Locate every blood parasite and identify its species.
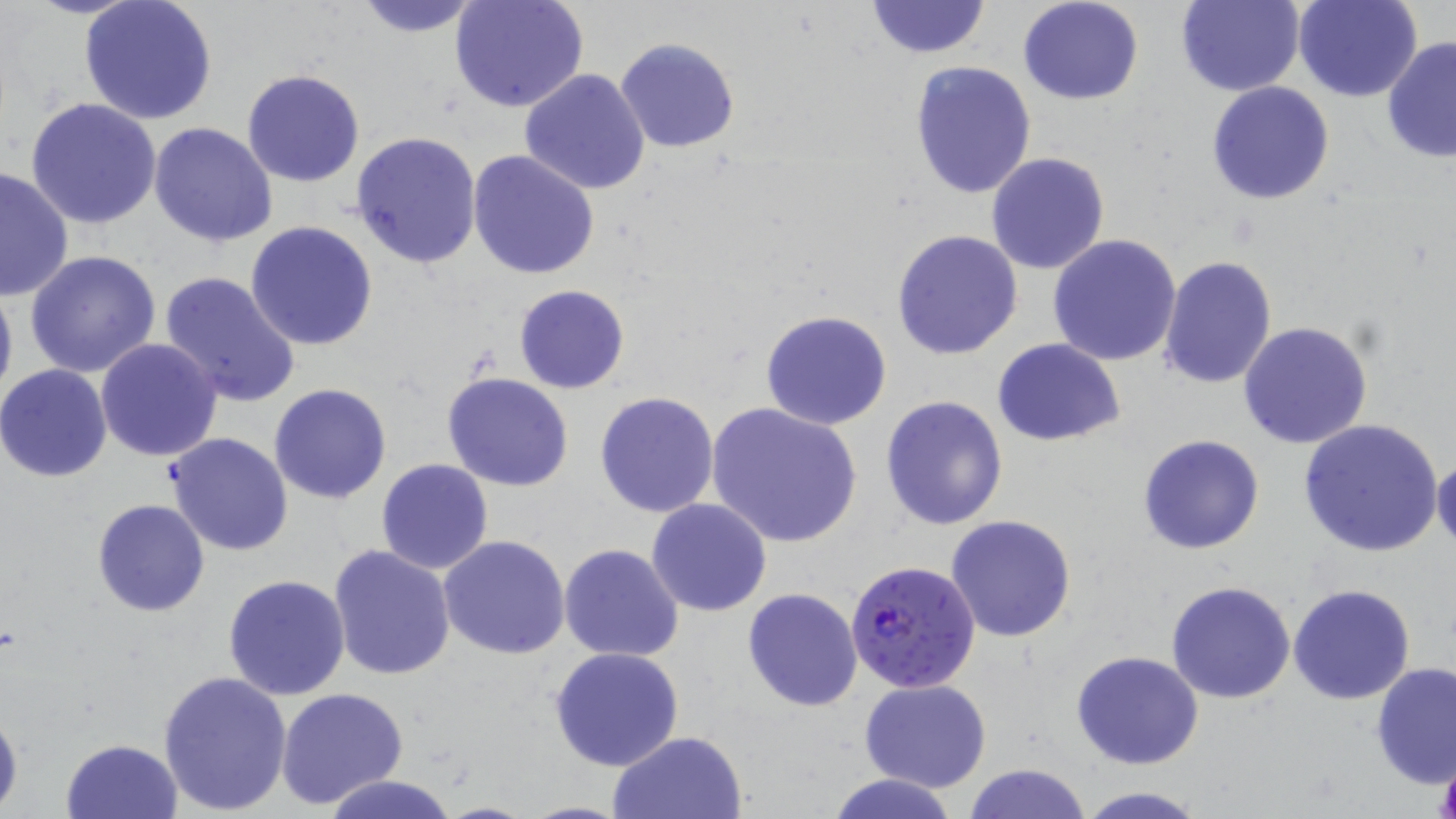
Approximate bounding boxes as [x1, y1, x2, y2] in pixels.
Plasmodium falciparum-infected red blood cells: [844, 556, 981, 692].
No Plasmodium ovale, Plasmodium malariae, Plasmodium vivax, Babesia divergens, or Trypanosoma brucei observed.

Uninfected red blood cell locations: [348, 0, 490, 37], [865, 0, 990, 59], [1017, 0, 1144, 106], [1176, 0, 1305, 96], [1294, 0, 1421, 102], [78, 1, 219, 125], [450, 1, 589, 113], [615, 37, 741, 154], [1381, 37, 1456, 163], [908, 61, 1036, 199], [241, 68, 365, 187], [519, 69, 650, 195], [1206, 81, 1335, 205], [27, 97, 163, 230], [148, 123, 277, 247], [350, 131, 482, 269], [467, 151, 599, 280], [986, 153, 1111, 275], [0, 165, 73, 302], [246, 221, 378, 352], [892, 229, 1022, 360], [1047, 234, 1181, 366], [26, 250, 162, 379], [1157, 256, 1278, 391], [157, 271, 301, 410], [0, 277, 17, 412], [515, 284, 630, 395], [760, 310, 891, 430], [1237, 321, 1373, 450], [992, 337, 1125, 447], [94, 338, 222, 462], [0, 364, 112, 484], [442, 372, 575, 492], [268, 382, 393, 505], [594, 391, 721, 518], [879, 395, 1009, 530], [706, 403, 862, 548], [1298, 419, 1444, 557], [166, 433, 293, 556], [1137, 434, 1265, 555], [376, 457, 494, 575], [1432, 457, 1456, 550], [647, 497, 772, 616], [92, 499, 210, 618], [945, 515, 1077, 642], [438, 535, 572, 659], [558, 543, 685, 662], [328, 546, 457, 683], [222, 575, 351, 701], [1166, 579, 1296, 703], [1288, 584, 1415, 703], [742, 588, 863, 711], [549, 647, 686, 772], [1070, 649, 1204, 770], [1371, 663, 1455, 788], [158, 670, 293, 816], [859, 678, 991, 792], [277, 688, 408, 809], [0, 706, 22, 813], [607, 730, 747, 818], [60, 738, 183, 819], [963, 761, 1093, 819], [827, 772, 961, 819], [320, 774, 457, 819], [1075, 785, 1207, 818], [432, 800, 538, 818], [519, 801, 633, 818]. Slide-level diagnosis: Plasmodium falciparum. Captured at 1000x magnification. Thin blood smear. May-Grünwald-Giemsa stain. Light microscopy. Image is 1456×819 pixels. Single field of view.